Report the malaria status of this cell.
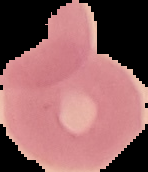

It is uninfected.

preparation = thin blood smear
image type = segmented cell region on a black background
image size = 148×172 pixels